Name the parasite shown.
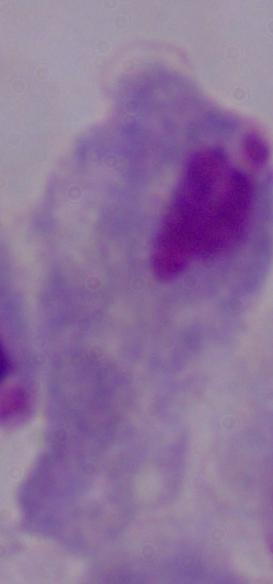
This is a trichomonad.

{
  "magnification": "1000x",
  "modality": "micrograph"
}